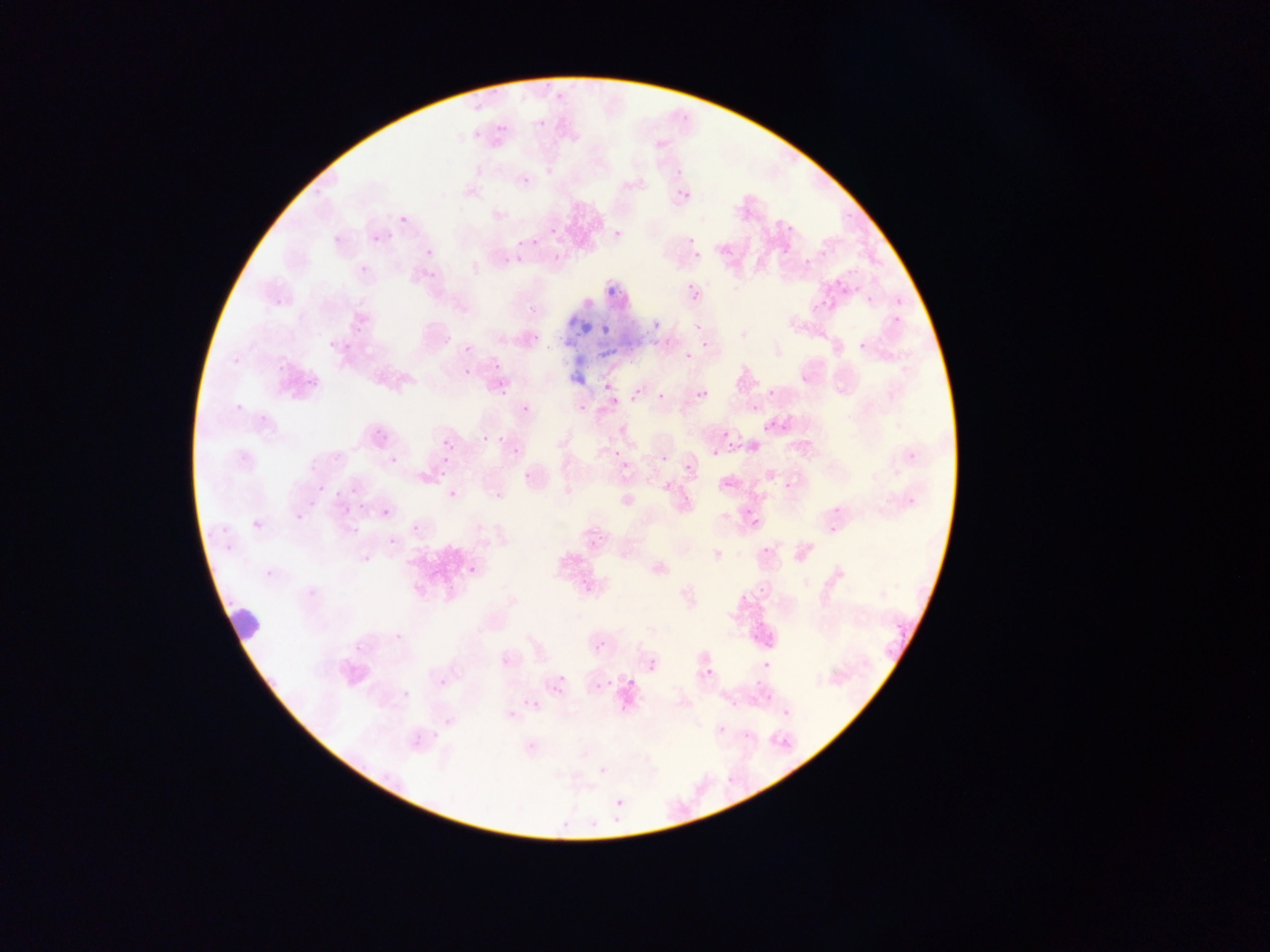
Approximate bounding boxes as left top right bottom in pixels.
Summary:
  - Plasmodium parasite locations: 496 124 506 134; 471 130 481 141; 521 175 532 186; 678 189 691 202; 399 216 407 225; 788 226 797 231; 549 227 559 237; 612 228 624 241; 371 234 381 244; 689 234 700 250; 688 236 697 245; 532 238 541 247; 423 247 430 256; 692 252 702 261; 515 256 525 265; 802 260 814 266; 428 273 439 279; 687 283 700 296; 687 286 704 304; 891 314 903 327; 651 319 663 333; 353 323 367 334; 601 324 611 335; 701 337 710 349; 857 340 868 352; 464 344 474 354; 684 350 694 360; 492 361 503 373; 463 368 473 378; 800 374 808 381; 304 375 318 391; 602 382 614 394; 499 387 512 399; 632 387 643 398; 767 387 778 398; 697 389 708 400; 657 392 666 401; 751 403 760 412; 578 404 587 413; 521 405 529 413; 761 420 768 431; 778 420 794 435; 723 431 731 439; 378 433 389 440; 481 434 487 444; 442 438 453 450; 511 443 519 458; 747 443 759 453; 612 448 622 458; 712 451 720 459; 906 451 915 460; 660 454 669 464; 387 457 397 466; 620 461 631 472; 684 463 694 473; 438 464 450 476; 521 469 535 484; 723 478 735 490; 318 479 330 494; 782 480 794 492; 350 486 360 496; 448 489 460 502; 336 490 348 499; 903 493 920 511; 829 504 844 513; 342 506 352 515; 381 508 391 519; 743 509 752 514; 295 513 303 522; 750 520 763 528; 350 524 361 537; 411 524 423 536; 828 527 838 535; 388 537 398 547; 761 545 772 556; 359 548 376 562; 467 565 478 576; 263 571 276 581; 579 578 591 586; 759 582 768 596; 392 633 402 639; 881 639 904 665; 355 640 364 655; 596 640 607 652; 647 659 659 673; 761 660 771 669; 702 666 715 679; 438 671 450 690; 753 677 765 689; 604 679 614 689; 595 682 606 693; 765 696 778 706; 528 699 542 712; 730 700 741 707; 506 709 519 721; 780 709 796 720; 432 729 440 743; 718 729 729 734; 598 765 609 777; 614 797 626 809 | approximate x y pixel centers of objects too small to bound: 824 302; 813 308; 377 433; 500 439; 742 598; 404 697; 745 737
  - Leukocyte locations: 220 608 266 653
  - Country: Ghana
  - Preparation: thin blood film
  - Image size: 1270×952 pixels
  - Capture: mobile-phone photograph through a microscope
  - Field of view: single